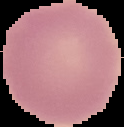

Summary:
  - Image type: cell region segmented out of the field of view; surrounding area masked to black
  - Image size: 124×127 pixels
  - Preparation: thin blood film
  - Malaria status: uninfected